Give the extent of all Babesia divergens-infected red blood cells.
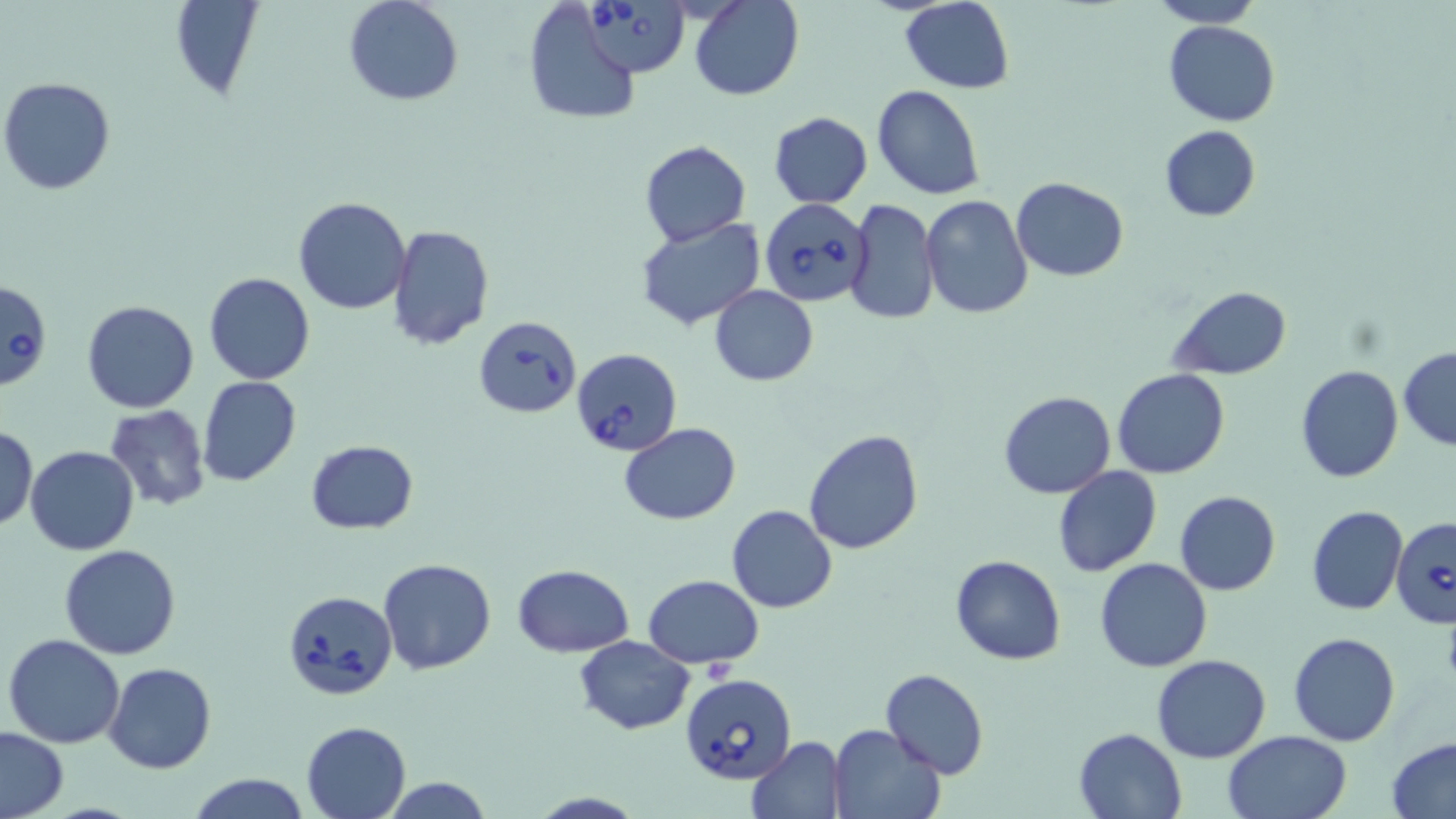

Approximate bounding boxes as named x1/y1/x2/y2 corners in pixels.
Babesia divergens-infected red blood cells: (x1=579, y1=0, x2=689, y2=77), (x1=759, y1=199, x2=872, y2=306), (x1=0, y1=281, x2=51, y2=390), (x1=475, y1=315, x2=582, y2=417), (x1=572, y1=347, x2=682, y2=457), (x1=1389, y1=516, x2=1456, y2=629), (x1=283, y1=590, x2=398, y2=700), (x1=680, y1=674, x2=797, y2=785).

Summary:
  - Uninfected red blood cell locations: (x1=167, y1=0, x2=265, y2=102), (x1=343, y1=0, x2=464, y2=106), (x1=690, y1=0, x2=804, y2=100), (x1=1150, y1=0, x2=1262, y2=27), (x1=900, y1=1, x2=1015, y2=93), (x1=521, y1=2, x2=642, y2=126), (x1=1163, y1=20, x2=1282, y2=127), (x1=1, y1=75, x2=117, y2=197), (x1=873, y1=84, x2=985, y2=200), (x1=768, y1=111, x2=873, y2=207), (x1=1158, y1=125, x2=1260, y2=222), (x1=640, y1=140, x2=750, y2=245), (x1=1011, y1=177, x2=1129, y2=281), (x1=920, y1=195, x2=1033, y2=318), (x1=292, y1=196, x2=412, y2=314), (x1=844, y1=199, x2=938, y2=324), (x1=635, y1=216, x2=764, y2=330), (x1=388, y1=226, x2=494, y2=349), (x1=205, y1=272, x2=314, y2=385), (x1=710, y1=285, x2=817, y2=385), (x1=1169, y1=286, x2=1293, y2=378), (x1=81, y1=300, x2=199, y2=413), (x1=1398, y1=348, x2=1456, y2=451), (x1=1296, y1=364, x2=1403, y2=483), (x1=1113, y1=369, x2=1230, y2=478), (x1=198, y1=377, x2=303, y2=487), (x1=998, y1=391, x2=1116, y2=499), (x1=104, y1=404, x2=212, y2=512), (x1=619, y1=421, x2=742, y2=526), (x1=1, y1=423, x2=38, y2=530), (x1=803, y1=429, x2=923, y2=555), (x1=306, y1=440, x2=419, y2=533), (x1=25, y1=445, x2=138, y2=555), (x1=1053, y1=465, x2=1162, y2=577), (x1=1174, y1=490, x2=1280, y2=596), (x1=726, y1=504, x2=838, y2=613), (x1=1307, y1=506, x2=1408, y2=616), (x1=59, y1=543, x2=181, y2=659), (x1=950, y1=554, x2=1066, y2=666), (x1=1095, y1=558, x2=1213, y2=673), (x1=377, y1=559, x2=496, y2=676), (x1=512, y1=564, x2=633, y2=657), (x1=643, y1=575, x2=765, y2=668), (x1=4, y1=632, x2=125, y2=749), (x1=1288, y1=632, x2=1399, y2=746), (x1=575, y1=635, x2=695, y2=735), (x1=1151, y1=654, x2=1271, y2=764), (x1=104, y1=662, x2=216, y2=774), (x1=879, y1=668, x2=989, y2=779), (x1=301, y1=720, x2=412, y2=819), (x1=828, y1=724, x2=945, y2=818), (x1=0, y1=726, x2=68, y2=819), (x1=1073, y1=727, x2=1187, y2=817), (x1=1224, y1=731, x2=1353, y2=819), (x1=746, y1=735, x2=847, y2=818), (x1=1386, y1=736, x2=1456, y2=818), (x1=185, y1=773, x2=310, y2=819), (x1=384, y1=778, x2=492, y2=817), (x1=526, y1=791, x2=646, y2=819)
  - Slide-level diagnosis: Babesia divergens
  - Preparation: thin blood smear
  - Field of view: single
  - Stain: May-Grünwald-Giemsa
  - Magnification: 1000x
  - Modality: light microscopy
  - Image size: 1456×819 pixels